Classify this cell by malaria status.
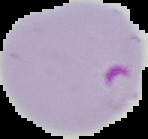
It is parasitized.

{
  "image_type": "cell region segmented out of the field of view; surrounding area masked to black",
  "image_size": "148×139 pixels",
  "preparation": "thin blood smear"
}